Classify this cell by malaria status.
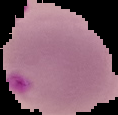
It is parasitized.

Image is 118×115 pixels. The area outside the segmented cell region is set to black. From a thin blood film.